Identify the parasite.
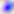
Toxoplasma gondii.

Summary:
  - Magnification: 400x
  - Modality: photomicrograph